Report the malaria status of this cell.
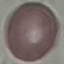
It is uninfected.

stain = Giemsa
preparation = thin blood film
capture = smartphone through the microscope eyepiece
image type = cell patch, automatically extracted from a larger field of view and resized to 64 × 64 pixels